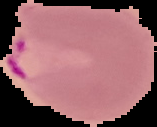
Summary:
  - Result: Plasmodium parasites detected
  - Preparation: thin blood smear
  - Image type: segmented cell region with the area outside set to black
  - Image size: 157×127 pixels